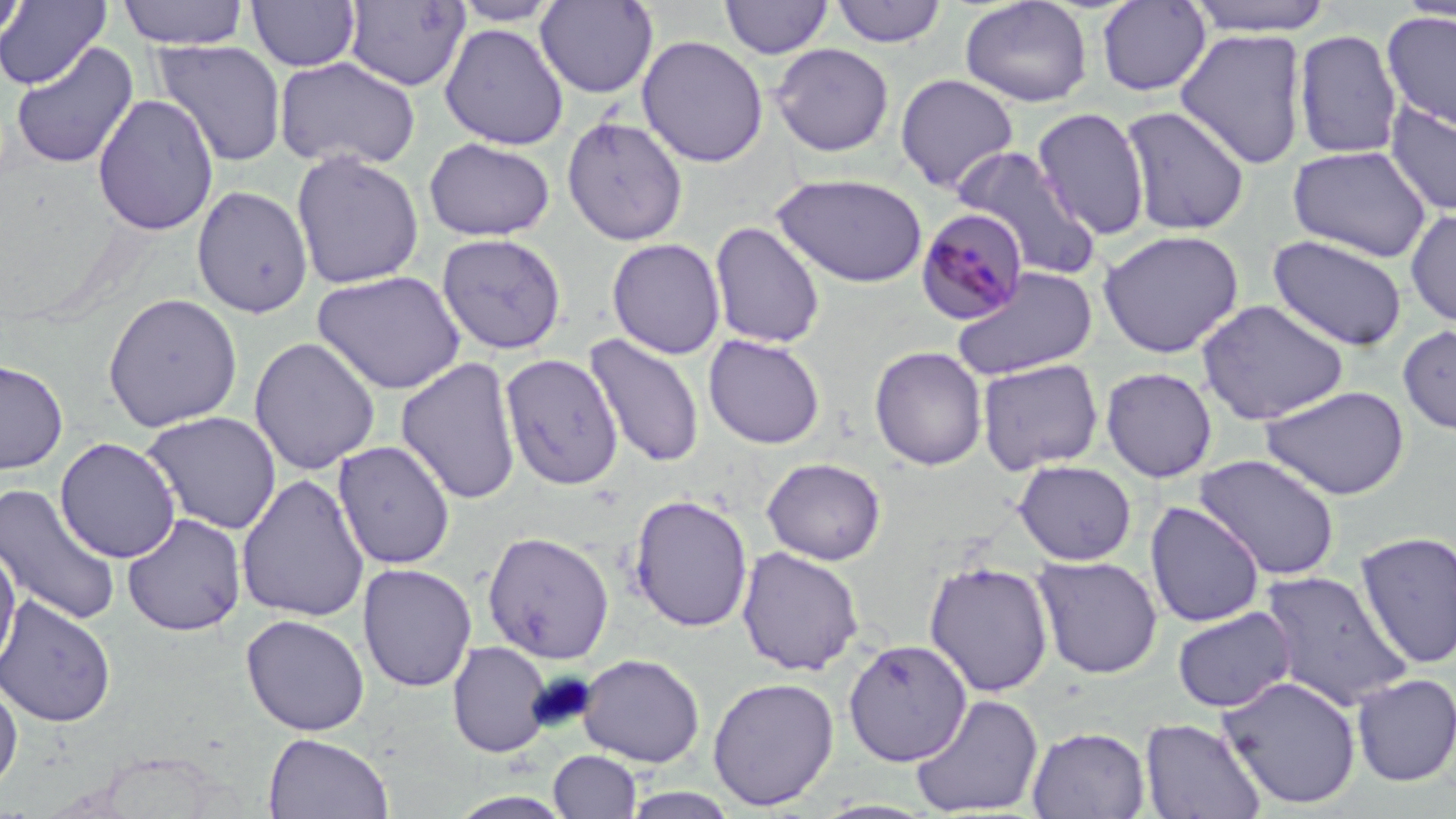 Approximate bounding boxes as (x1,y1)-(x2,y2) corner pairs in pixels. Plasmodium malariae-infected red blood cell locations: (915,207)-(1030,325). Uninfected red blood cell locations: (0,0)-(28,46), (118,0)-(249,49), (246,0)-(361,72), (720,0)-(834,59), (830,0)-(947,48), (959,0)-(1093,108), (1184,0)-(1336,36), (0,1)-(111,89), (343,1)-(470,92), (451,1)-(563,27), (535,1)-(658,99), (1095,1)-(1213,97), (1394,1)-(1456,23), (1382,10)-(1456,133), (439,23)-(569,150), (1174,28)-(1309,170), (1293,29)-(1403,161), (636,35)-(769,168), (152,39)-(287,167), (11,41)-(139,169), (770,43)-(895,157), (274,55)-(421,171), (895,74)-(1019,193), (92,93)-(219,236), (1384,100)-(1456,217), (1118,105)-(1252,236), (1031,107)-(1151,240), (561,114)-(689,246), (424,136)-(556,241), (1287,145)-(1434,263), (954,146)-(1101,280), (290,148)-(425,290), (771,172)-(928,288), (192,185)-(313,318), (1404,208)-(1456,327), (709,221)-(825,349), (1097,229)-(1244,358), (437,233)-(567,356), (1267,234)-(1408,351), (607,237)-(726,359), (951,266)-(1098,381), (312,270)-(466,395), (102,292)-(243,432), (1196,299)-(1349,425), (1398,324)-(1456,436), (583,333)-(705,469), (702,334)-(826,449), (248,336)-(381,475), (869,345)-(987,470), (500,352)-(623,490), (395,356)-(522,505), (0,358)-(69,474), (976,359)-(1104,475), (1100,366)-(1218,483), (1260,384)-(1410,499), (140,410)-(282,534), (55,437)-(181,563), (332,440)-(456,570), (1194,453)-(1341,580), (762,457)-(887,565), (1013,460)-(1137,565), (235,472)-(371,623), (0,482)-(123,626), (628,494)-(753,632), (1145,501)-(1265,628), (122,513)-(247,636), (481,530)-(615,664), (1353,530)-(1456,669), (0,541)-(21,674), (736,546)-(864,676), (1031,554)-(1163,679), (923,560)-(1054,697), (356,562)-(477,693), (1258,569)-(1412,711), (0,594)-(117,728), (1172,606)-(1296,713), (240,613)-(370,736), (843,639)-(973,766), (447,640)-(553,758), (576,653)-(705,768), (1351,672)-(1456,787), (1217,673)-(1363,811), (706,676)-(840,811), (0,678)-(23,795), (909,693)-(1044,816), (1140,717)-(1267,819), (1027,725)-(1150,819), (262,732)-(394,819), (548,750)-(642,818), (618,787)-(743,818). Slide-level diagnosis: Plasmodium malariae. Thin blood smear. 1000x magnification. Image is 1456×819 pixels. Optical microscopy. Single field of view. May-Grünwald-Giemsa stain.